Assess this cell for malaria.
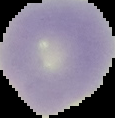

It is uninfected.

From a thin blood film. Image is 115×118 pixels. The area outside the segmented cell region is set to black.